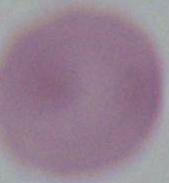
{
  "modality": "micrograph",
  "identification": "red blood cell",
  "magnification": "1000x"
}